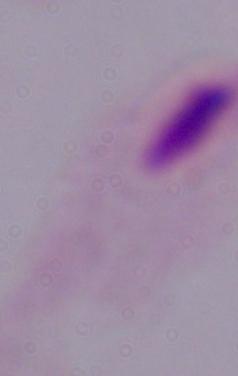 1000x magnification. Micrograph. A trichomonad is seen.